Assess this cell for malaria.
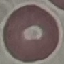

It is uninfected.

Giemsa stain. Automatically extracted cell patch, resized to 64 × 64 pixels. Acquired by smartphone through the microscope eyepiece. Thin blood smear.